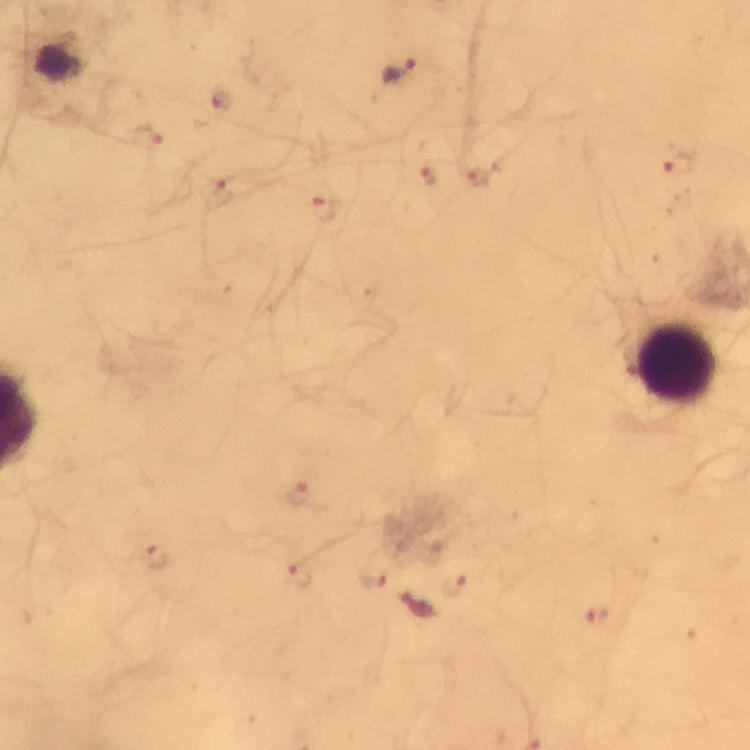

Approximate object centers, in pixels from the top-left corner. Plasmodium parasite locations: (x=400, y=71), (x=222, y=99), (x=145, y=138), (x=681, y=162), (x=427, y=173), (x=479, y=176), (x=220, y=188), (x=324, y=209), (x=298, y=491), (x=154, y=558), (x=373, y=576), (x=297, y=577), (x=453, y=585), (x=415, y=606), (x=596, y=616). Leukocyte locations: (x=677, y=364). Photographed with a smartphone mounted on the microscope. A crop from one field of view. Giemsa stain. 100x magnification. From a malaria diagnostic workup. Image is 750×750 pixels. Immersion oil was used. Thick blood smear.